Comment on the morphology of the erythrocytes.
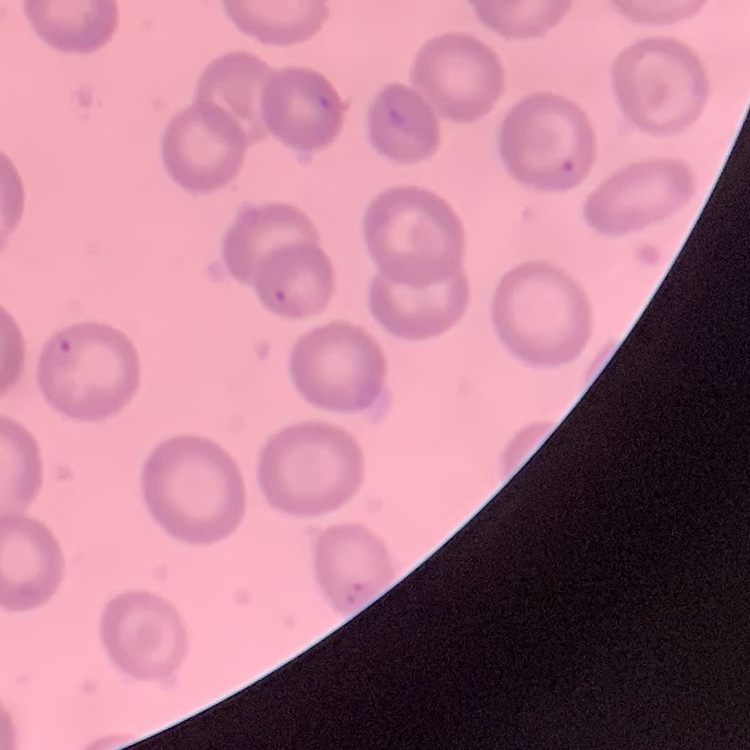

No rouleaux formation.

Summary:
  - Image type: square crop of a larger photomicrograph
  - Stain: Field's or Giemsa
  - Preparation: thin peripheral smear